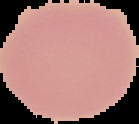

The area outside the segmented cell region is set to black. From a thin blood smear. Image is 139×124 pixels. Result: no malaria parasites seen.